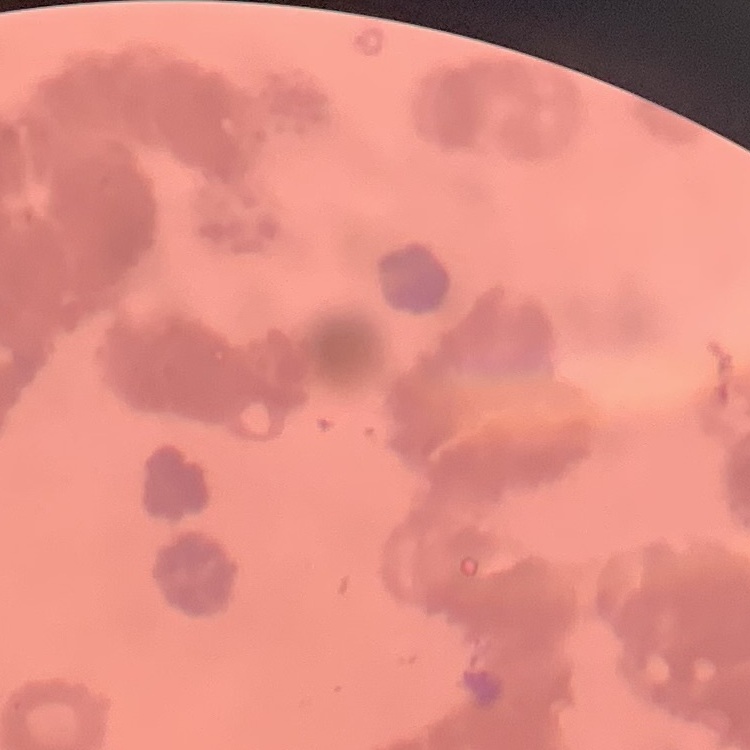
The red blood cells show rouleaux formation. One tile cut from a larger photomicrograph. Field's or Giemsa stain. Thin blood smear.